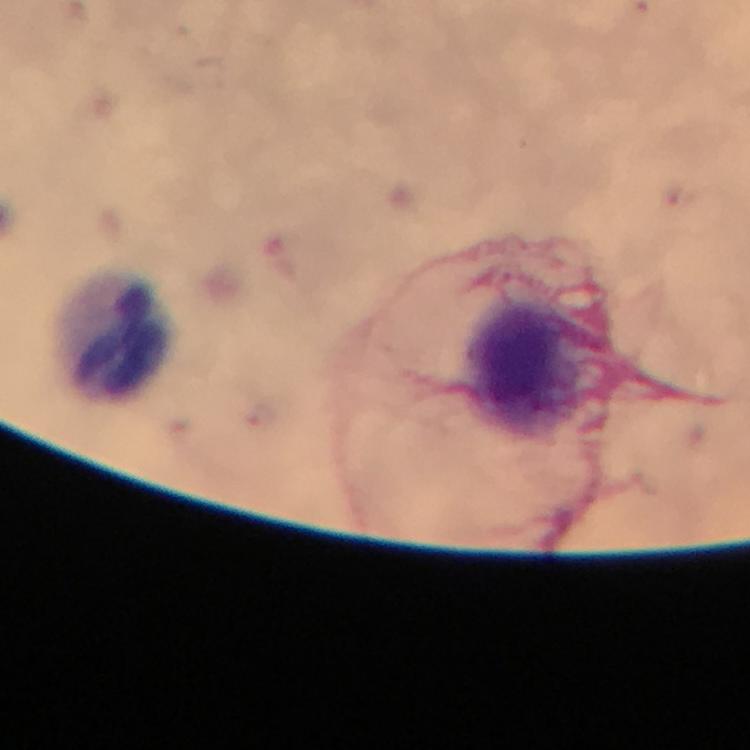

Approximate centers as {x, y} in pixels.
Summary:
  - Leukocyte locations: {114, 332}, {524, 364}
  - Stain: Giemsa
  - Cropped from: one field of view
  - Magnification: 100x
  - Capture: smartphone photograph through a microscope
  - Preparation: thick smear
  - Immersion oil: used
  - Image size: 750×750 pixels
  - Context: from a malaria diagnostic workup
  - Plasmodium parasites: none seen